Report the malaria status of this cell.
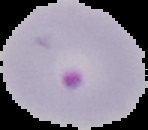
Parasitized.

image size = 148×130 pixels
preparation = thin blood film
image type = segmented cell region with the area outside set to black